Name the parasite shown.
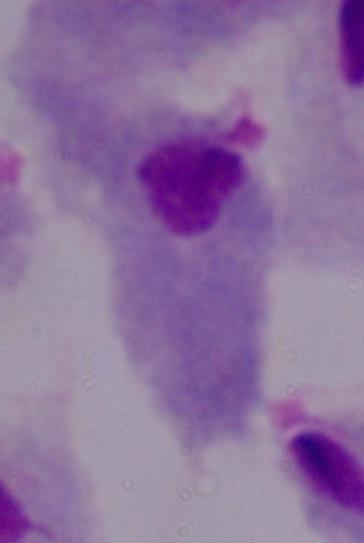
This is a trichomonad.

Micrograph. 1000x magnification.